Locate every uninfected red blood cell.
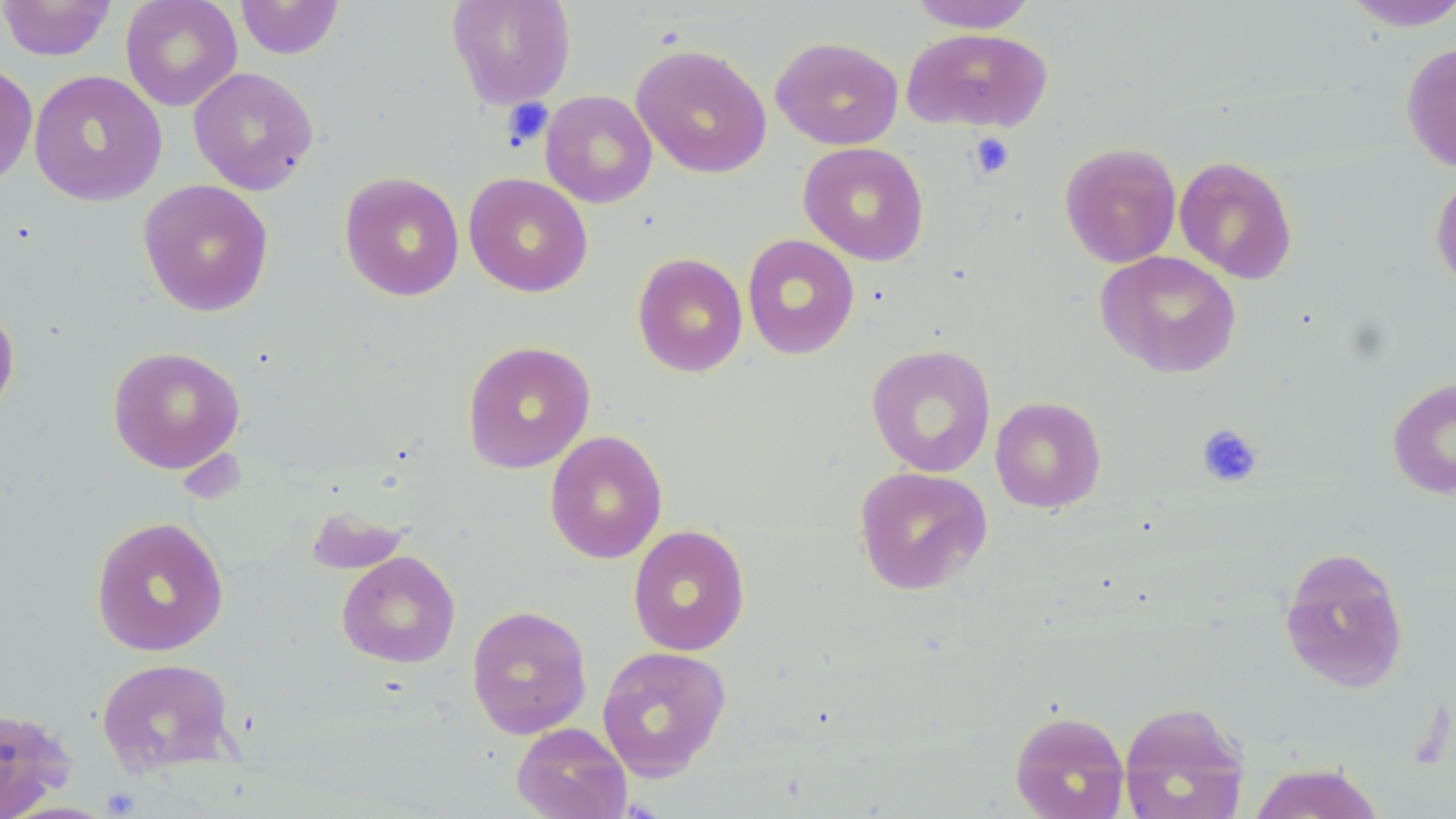
Approximate bounding boxes as [x1, y1, x2, y2] in pixels.
Uninfected red blood cells: [0, 0, 117, 61], [121, 0, 242, 111], [234, 0, 345, 60], [446, 0, 577, 110], [907, 0, 1038, 33], [1337, 1, 1456, 32], [901, 27, 1053, 132], [770, 36, 904, 150], [1401, 42, 1456, 174], [631, 43, 772, 178], [0, 61, 37, 191], [188, 66, 319, 195], [28, 69, 167, 207], [540, 90, 657, 208], [798, 141, 930, 266], [1059, 141, 1181, 268], [1174, 155, 1298, 285], [338, 171, 465, 301], [463, 172, 593, 297], [1430, 172, 1456, 293], [137, 179, 275, 317], [741, 234, 860, 360], [1095, 250, 1242, 379], [632, 252, 748, 377], [0, 299, 20, 425], [461, 340, 596, 474], [865, 344, 996, 478], [107, 346, 245, 474], [1387, 376, 1456, 500], [990, 396, 1107, 513], [544, 430, 668, 564], [853, 465, 993, 595], [304, 505, 411, 575], [90, 515, 230, 657], [627, 525, 750, 656], [1278, 546, 1409, 693], [337, 550, 460, 668], [466, 604, 592, 739], [596, 645, 732, 781], [95, 657, 237, 776], [1119, 701, 1250, 819], [0, 705, 76, 819], [1009, 709, 1130, 819], [511, 722, 631, 819], [1247, 761, 1384, 818].

Summary:
  - Platelet locations: [502, 98, 554, 150], [968, 132, 1015, 180], [1196, 423, 1264, 487]
  - Slide-level diagnosis: negative for blood parasites
  - Magnification: 1000x
  - Field of view: one of a larger specimen
  - Preparation: thin blood film
  - Modality: light microscopy
  - Image size: 1456×819 pixels
  - Stain: May-Grünwald-Giemsa